Point out each Plasmodium parasite.
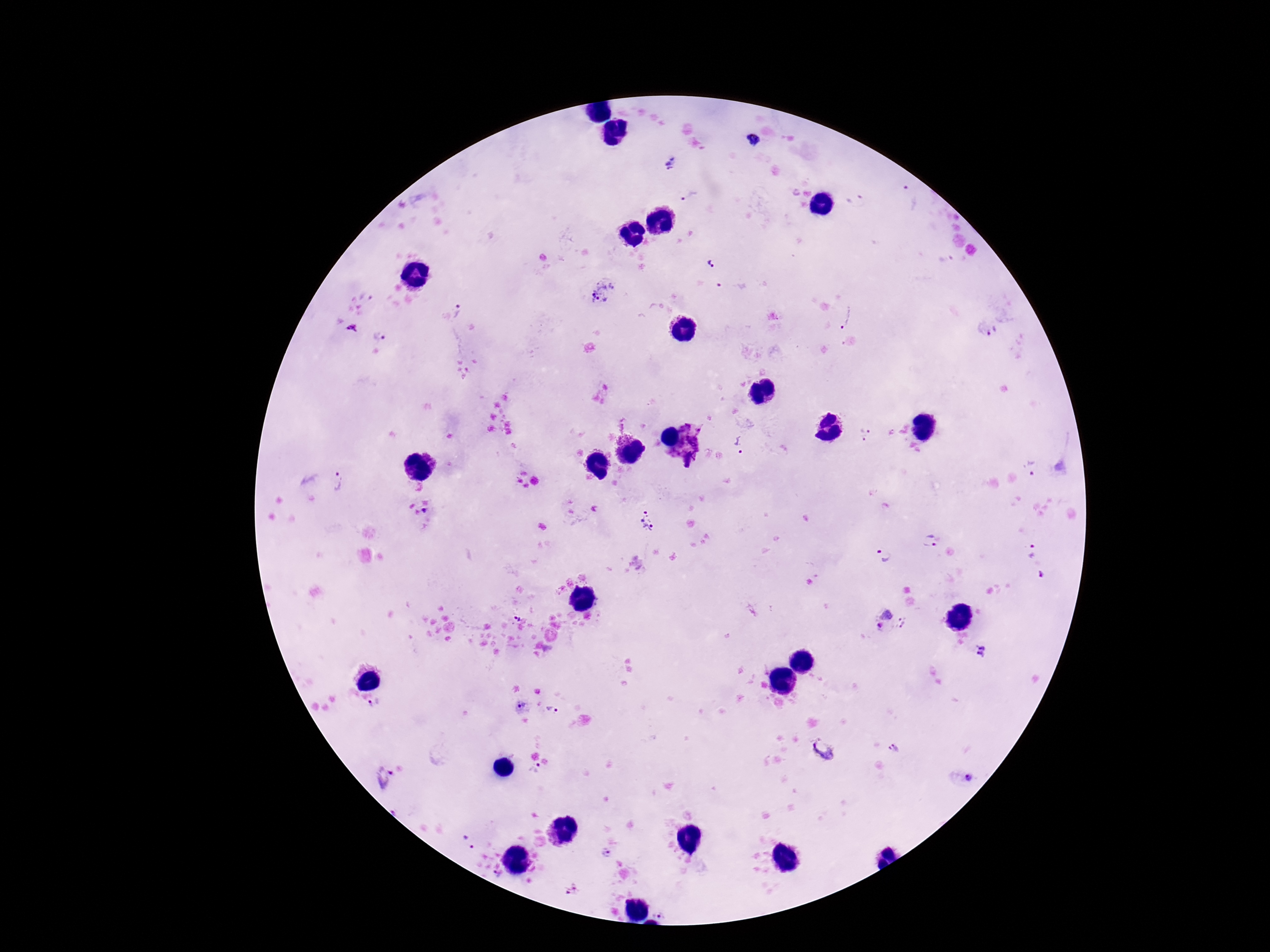
Approximate centers as (x, y) in pixels.
Plasmodium parasites: (754, 141), (672, 163), (690, 196), (909, 197), (857, 201), (712, 263), (604, 292), (460, 312), (848, 316), (353, 328), (987, 330), (380, 337), (622, 422), (685, 428), (699, 429), (867, 434), (623, 438), (694, 441), (741, 446), (689, 459), (1032, 469), (340, 483), (425, 512), (647, 521), (928, 541), (1031, 551), (884, 555), (887, 614), (516, 617), (904, 622), (879, 626), (980, 651), (376, 706), (517, 706), (552, 710), (895, 746), (824, 750), (536, 772), (381, 776), (468, 843), (607, 854), (573, 889), (662, 913).

image size = 1270×952 pixels
preparation = thick blood film
patient malaria status = infected
field of view = single
capture = smartphone camera through the microscope eyepiece
magnification = 100x
stain = Giemsa